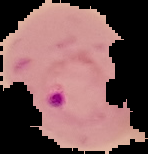

malaria status = parasitized
preparation = thin blood smear
image type = segmented cell region on a black background
image size = 148×154 pixels